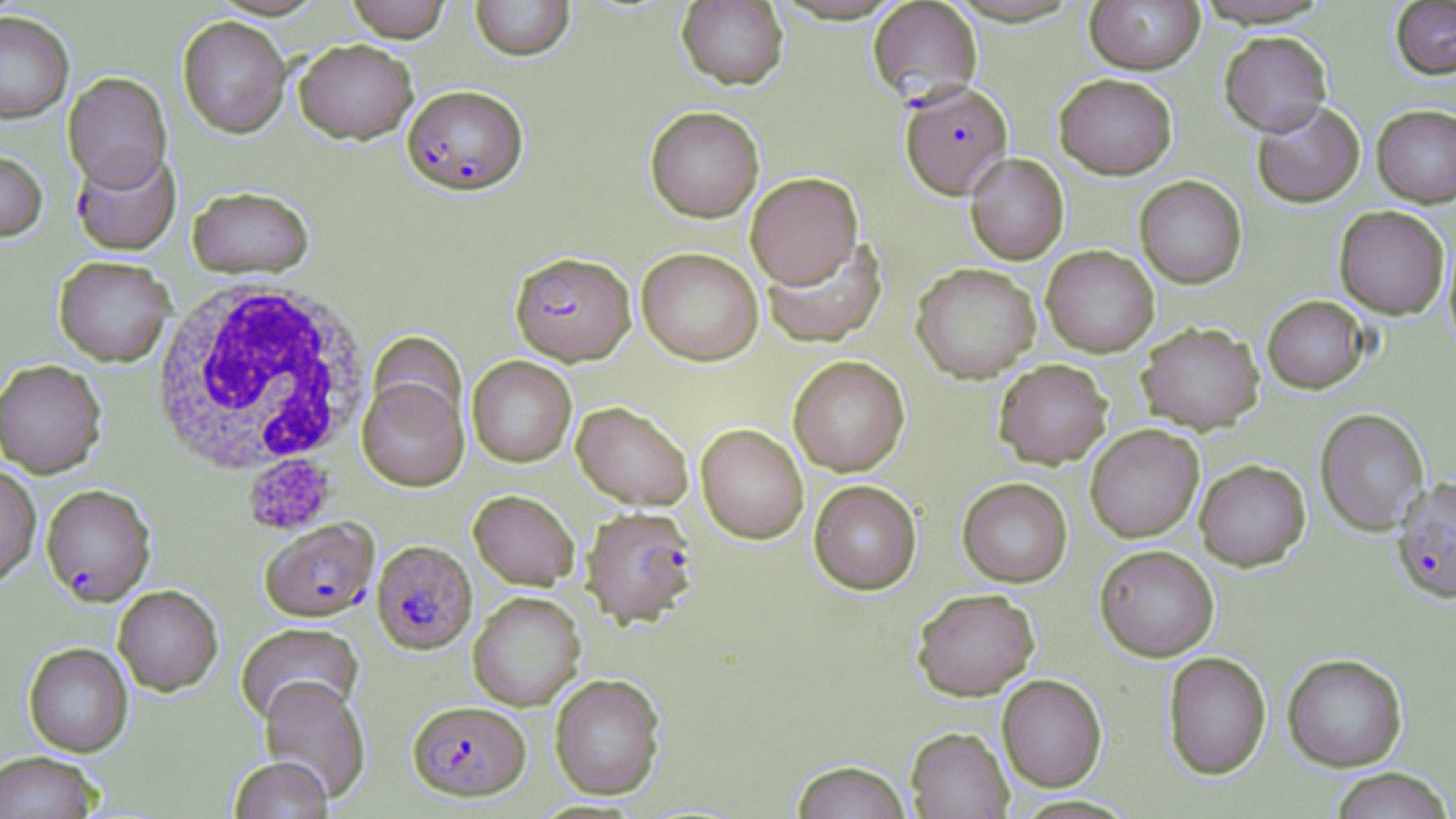

Summary:
  - Coordinate format: approximate bounding boxes as [x1, y1, x2, y2] in pixels
  - Platelet locations: [244, 453, 334, 535]
  - White blood cell locations: [148, 279, 374, 484]
  - Plasmodium falciparum-infected red blood cell locations: [869, 1, 983, 107], [900, 81, 1012, 199], [402, 85, 528, 195], [71, 147, 181, 255], [510, 251, 636, 365], [1392, 477, 1456, 603], [41, 484, 156, 606], [580, 505, 698, 627], [261, 518, 378, 621], [372, 540, 477, 653], [408, 700, 530, 800]
  - Uninfected red blood cell locations: [345, 0, 453, 42], [470, 0, 575, 61], [676, 0, 788, 90], [1085, 0, 1204, 74], [1190, 0, 1334, 27], [1391, 1, 1456, 78], [0, 12, 74, 124], [178, 16, 291, 137], [1220, 31, 1331, 135], [294, 39, 418, 143], [63, 72, 171, 190], [1054, 73, 1177, 179], [1252, 100, 1365, 208], [1372, 104, 1456, 207], [645, 106, 764, 222], [0, 149, 47, 242], [965, 153, 1069, 264], [745, 172, 863, 288], [1135, 175, 1247, 288], [187, 185, 315, 279], [1334, 206, 1450, 319], [1444, 229, 1456, 353], [761, 235, 888, 348], [1041, 245, 1159, 357], [636, 247, 763, 365], [53, 256, 176, 366], [911, 262, 1041, 383], [1262, 295, 1370, 393], [1137, 322, 1264, 433], [368, 331, 467, 432], [788, 355, 910, 476], [467, 356, 576, 467], [0, 359, 107, 477], [994, 360, 1112, 468], [357, 377, 469, 491], [572, 401, 694, 509], [1315, 408, 1429, 534], [696, 423, 808, 543], [1085, 425, 1204, 542], [1194, 459, 1310, 570], [0, 464, 40, 589], [957, 478, 1073, 587], [809, 480, 922, 595], [469, 490, 580, 589], [1095, 544, 1219, 661], [113, 585, 223, 695], [912, 588, 1040, 700], [468, 591, 585, 710], [235, 623, 364, 725], [23, 643, 133, 757], [1163, 652, 1271, 779], [1282, 653, 1407, 771], [550, 673, 666, 799], [997, 674, 1107, 792], [259, 677, 371, 802], [906, 727, 1013, 818], [0, 751, 104, 819], [228, 757, 333, 818], [790, 760, 911, 819], [1329, 768, 1454, 819]
  - Slide-level diagnosis: Plasmodium falciparum
  - Stain: May-Grünwald-Giemsa
  - Magnification: 1000x
  - Preparation: thin blood smear
  - Image size: 1456×819 pixels
  - Field of view: single
  - Modality: optical microscopy